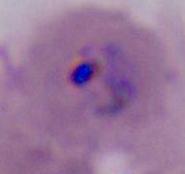

Photomicrograph. Captured at either 400x or 1000x magnification. A Plasmodium parasite is seen.